Report the malaria status of this cell.
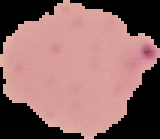

It is parasitized.

image size = 160×139 pixels
preparation = thin blood smear
image type = segmented cell region with the area outside set to black